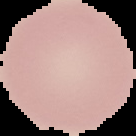

Summary:
  - Result: no malaria parasites detected
  - Image size: 136×136 pixels
  - Image type: segmented cell region on a black background
  - Preparation: thin blood smear